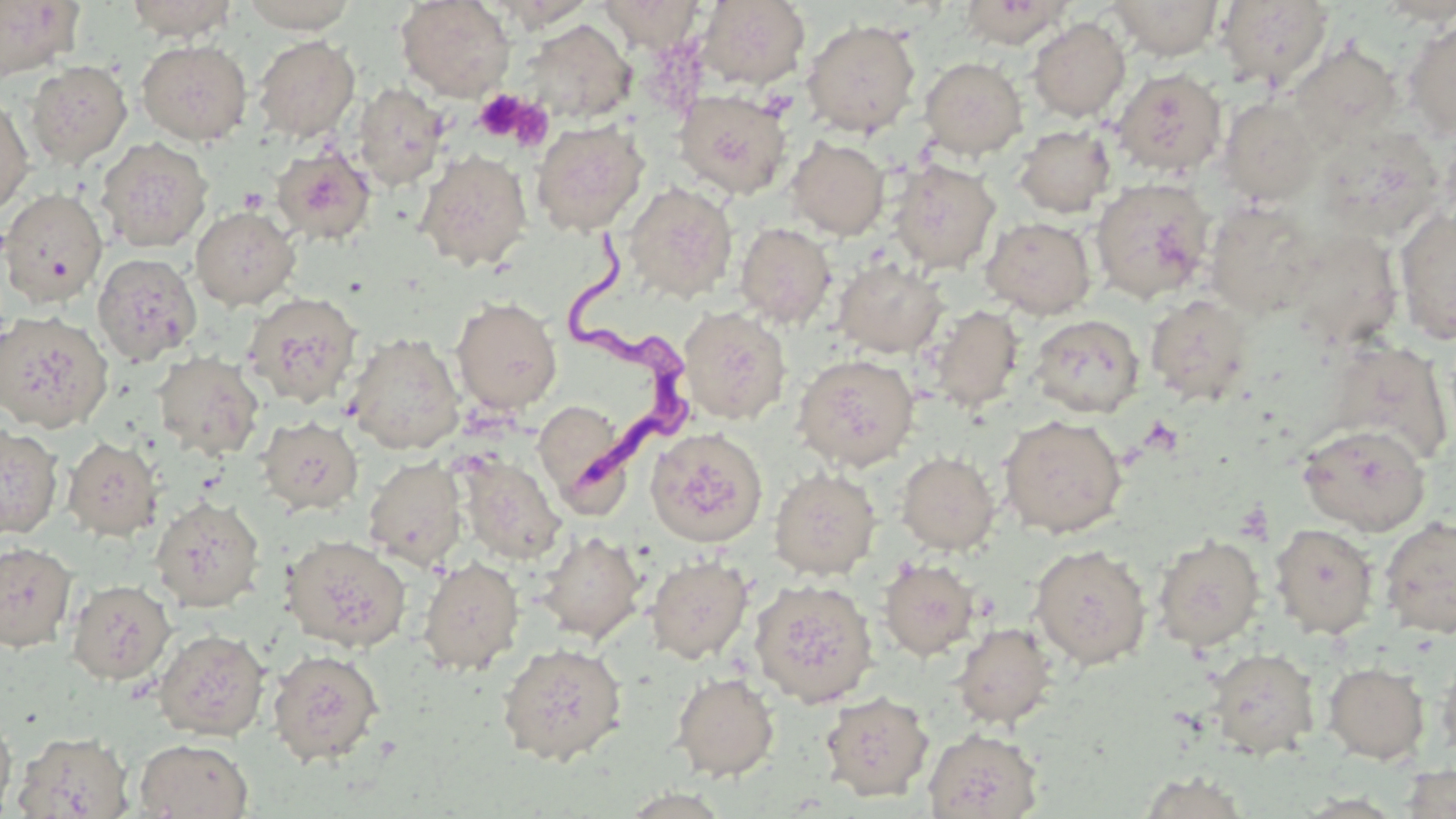

slide-level diagnosis = Trypanosoma brucei
field of view = one of a larger specimen
Trypanosoma brucei locations = approximate bounding boxes as [x1, y1, x2, y2] in pixels: [568, 223, 686, 495]
stain = May-Grünwald-Giemsa
uninfected red blood cell locations = approximate bounding boxes as [x1, y1, x2, y2] in pixels: [124, 0, 238, 42], [238, 0, 361, 33], [396, 0, 515, 101], [597, 0, 704, 51], [959, 0, 1072, 48], [1216, 0, 1334, 90], [0, 1, 83, 79], [490, 1, 595, 30], [698, 1, 810, 89], [1107, 1, 1225, 60], [1028, 17, 1130, 121], [1403, 17, 1456, 141], [802, 18, 921, 137], [522, 19, 636, 124], [253, 35, 360, 142], [136, 39, 252, 146], [1284, 42, 1403, 151], [919, 57, 1027, 159], [25, 60, 132, 169], [1113, 68, 1227, 178], [353, 83, 449, 191], [674, 89, 792, 199], [0, 92, 35, 217], [1218, 95, 1322, 206], [530, 119, 649, 236], [1013, 124, 1115, 217], [1315, 124, 1447, 244], [786, 136, 890, 239], [95, 137, 213, 253], [271, 145, 375, 245], [416, 149, 532, 271], [889, 159, 1001, 274], [1090, 176, 1217, 304], [623, 181, 738, 302], [0, 188, 108, 308], [1204, 199, 1320, 319], [191, 206, 300, 310], [1394, 208, 1456, 345], [980, 216, 1097, 319], [735, 222, 837, 329], [1285, 228, 1404, 350], [91, 252, 202, 365], [833, 258, 949, 358], [242, 291, 364, 409], [1145, 294, 1254, 405], [452, 297, 562, 414], [925, 305, 1025, 414], [678, 306, 791, 426], [0, 310, 114, 433], [1030, 314, 1144, 418], [345, 333, 465, 454], [1326, 339, 1453, 466], [153, 351, 264, 460], [792, 353, 919, 471], [532, 399, 630, 504], [999, 414, 1128, 538], [257, 415, 364, 516], [0, 423, 63, 539], [1297, 423, 1431, 536], [645, 427, 768, 547], [62, 436, 164, 541], [896, 452, 1001, 555], [457, 456, 566, 565], [364, 457, 468, 571], [769, 467, 880, 579], [150, 496, 265, 612], [1379, 515, 1456, 639], [1269, 523, 1378, 639], [534, 531, 647, 644], [281, 534, 412, 652], [1152, 534, 1265, 651], [0, 542, 77, 652], [1028, 543, 1152, 669], [645, 554, 754, 664], [417, 556, 525, 676], [878, 558, 981, 660], [749, 578, 878, 707], [66, 579, 176, 685], [952, 622, 1056, 729], [153, 628, 270, 741], [497, 642, 627, 765], [1436, 645, 1456, 766], [1205, 647, 1320, 760], [267, 649, 384, 766], [1323, 662, 1430, 764], [671, 671, 780, 781], [820, 691, 934, 801], [0, 712, 17, 818], [923, 728, 1043, 818], [12, 731, 133, 818], [134, 738, 253, 819], [1134, 771, 1255, 818]
magnification = 1000x
platelet locations = approximate bounding boxes as [x1, y1, x2, y2] in pixels: [474, 90, 532, 142], [503, 98, 555, 152], [238, 187, 269, 214]
preparation = thin blood smear
image size = 1456×819 pixels
modality = optical microscopy